Locate and identify every blood parasite.
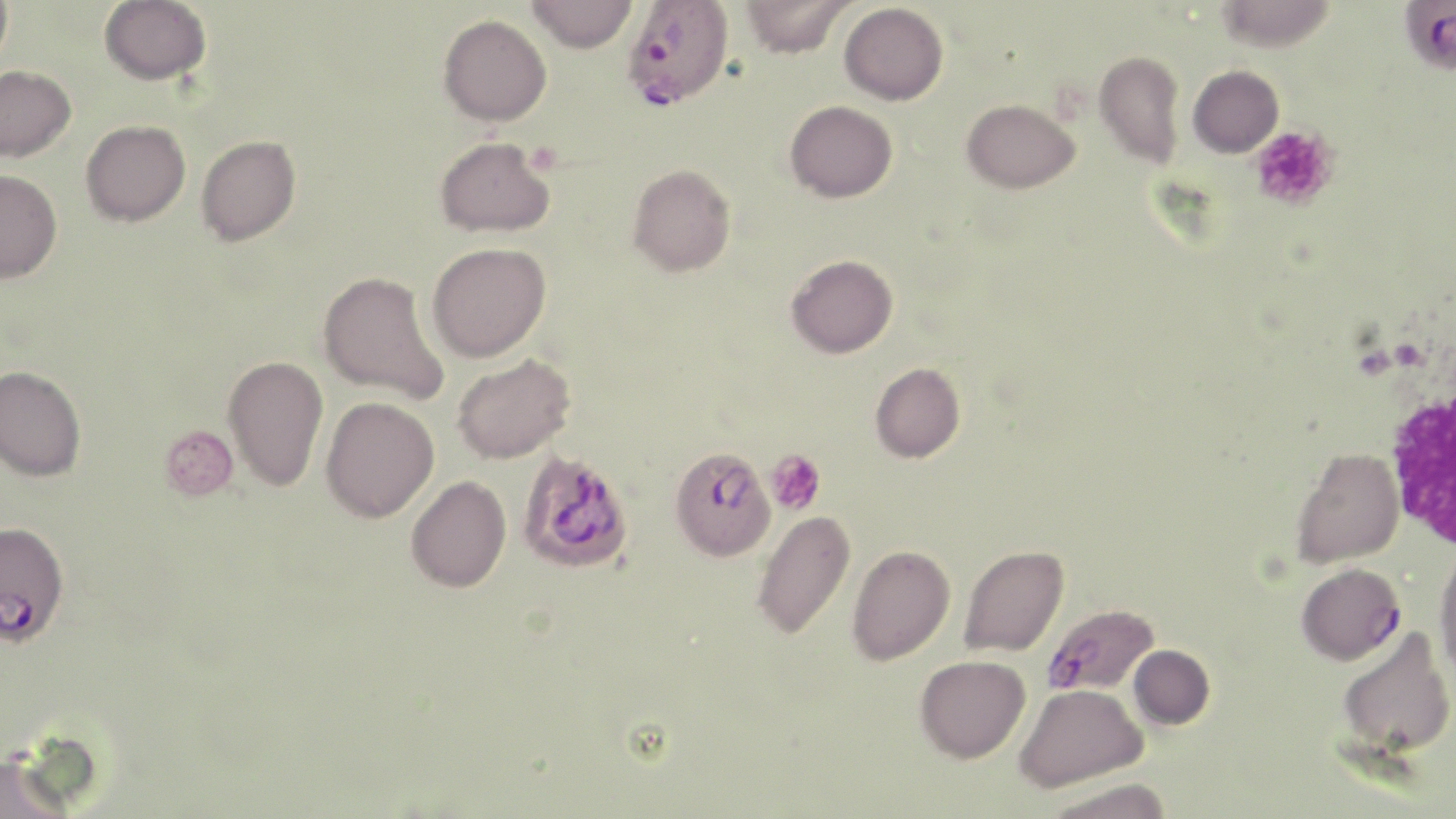
Approximate bounding boxes as (x1,y1)-(x2,y2) corner pairs in pixels.
Plasmodium falciparum-infected red blood cells: (624,0)-(735,110), (1401,1)-(1456,74), (669,447)-(776,561), (516,450)-(634,574), (0,519)-(75,652), (1296,563)-(1404,664), (1043,603)-(1159,697).
No Plasmodium ovale, Plasmodium malariae, Plasmodium vivax, Babesia divergens, or Trypanosoma brucei observed.

Summary:
  - Platelet locations: (1250,126)-(1337,210), (1391,338)-(1429,371), (159,424)-(238,501), (764,450)-(826,514)
  - Uninfected red blood cell locations: (0,0)-(12,73), (99,0)-(212,85), (526,0)-(637,53), (740,0)-(854,58), (1215,0)-(1338,52), (839,2)-(948,105), (438,14)-(551,126), (1093,49)-(1186,168), (0,65)-(76,162), (1188,65)-(1283,157), (961,98)-(1080,193), (785,100)-(898,202), (80,119)-(191,226), (196,135)-(301,246), (435,136)-(555,237), (627,163)-(736,277), (0,169)-(62,283), (427,241)-(551,361), (786,254)-(898,359), (318,270)-(448,404), (452,353)-(575,464), (223,354)-(328,491), (870,362)-(966,463), (0,366)-(86,482), (321,396)-(439,523), (1291,447)-(1404,568), (406,475)-(511,592), (752,509)-(856,641), (847,544)-(956,666), (959,545)-(1069,658), (1434,549)-(1456,684), (1336,627)-(1455,759), (1129,644)-(1214,729), (914,655)-(1030,763), (1014,683)-(1147,792), (0,751)-(78,819), (1041,778)-(1173,819)
  - White blood cell locations: (1385,382)-(1456,556)
  - Slide-level diagnosis: Plasmodium falciparum
  - Field of view: single
  - Preparation: thin blood film
  - Image size: 1456×819 pixels
  - Magnification: 1000x
  - Stain: May-Grünwald-Giemsa
  - Modality: optical microscopy